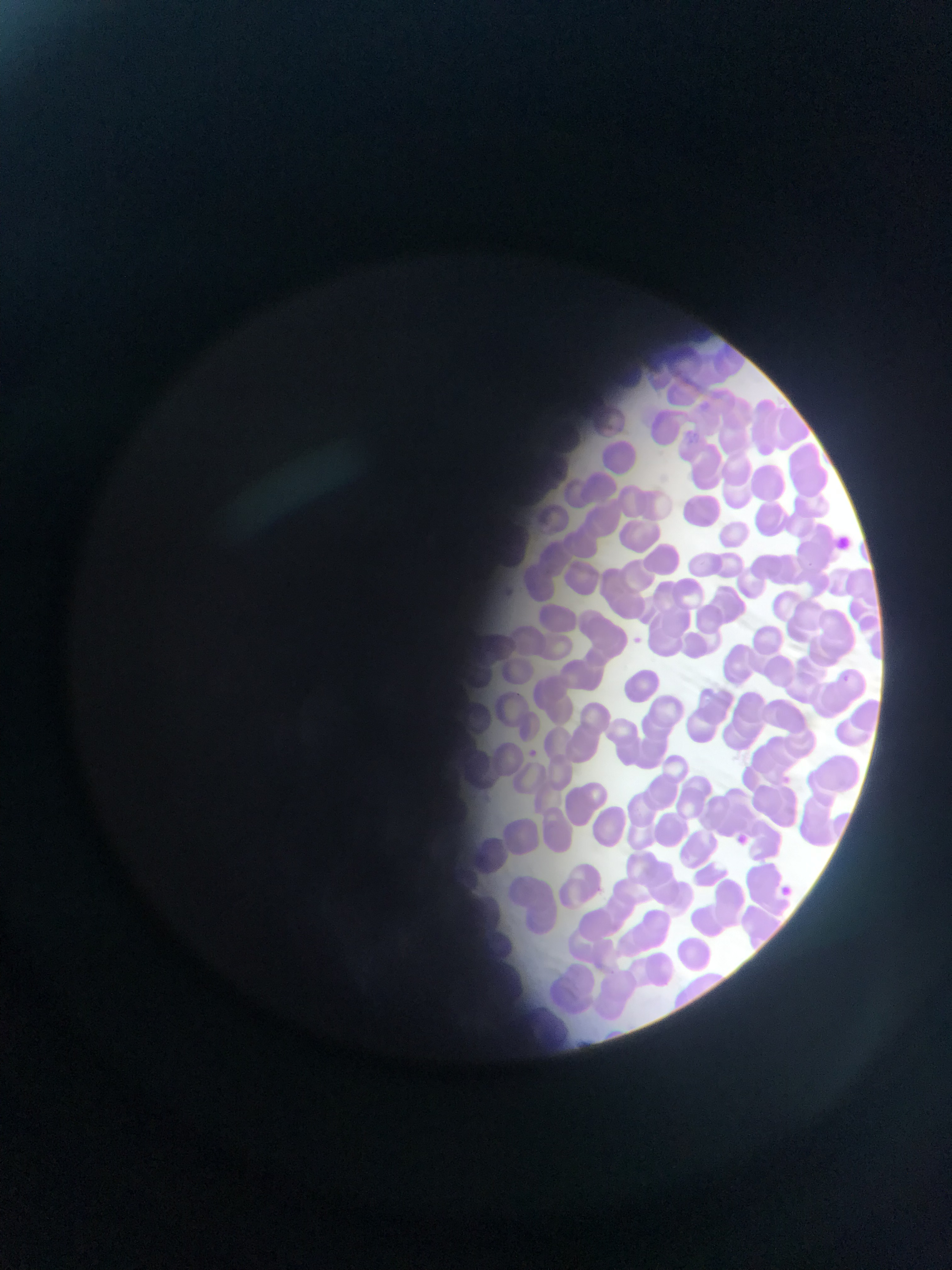
Approximate bounding boxes as left top right bottom in pixels. Malaria parasite locations: 506 585 531 608; 623 632 653 646; 521 745 553 768; 722 822 746 844; 779 879 795 897. Single field of view. Image is 952×1270 pixels. Sample from Ghana. Photographed through a microscope with a mobile-phone camera. Thin blood film.